Outline every leukocyte.
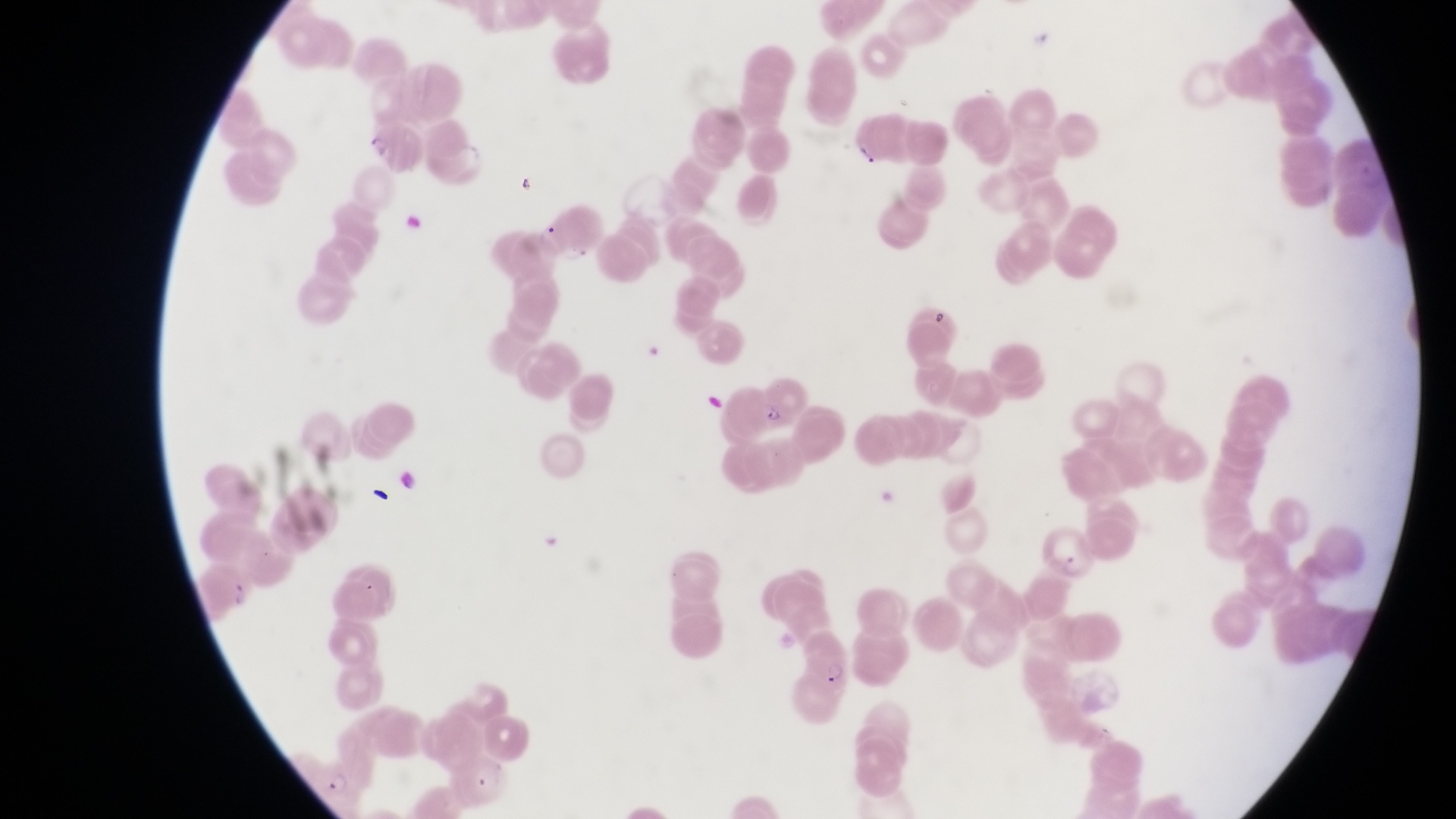
No leukocytes observed.

{
  "magnification": "1000x",
  "country": "Uganda",
  "preparation": "thin blood film",
  "field_of_view": "single",
  "artifact_platelet_like_body_stain_precipitate_or_debris_locations": "approximate bounding boxes as [left, top, right, bottom] in pixels: [856, 139, 883, 175], [512, 168, 545, 205], [925, 300, 958, 332], [367, 481, 399, 520]",
  "image_size": "1456×819 pixels",
  "parasitised_red_blood_cell_locations": "approximate bounding boxes as [left, top, right, bottom] in pixels: [753, 366, 808, 424], [798, 631, 851, 695]",
  "capture": "smartphone photograph through the eyepiece of an Olympus CX-23 microscope",
  "trophozoite_locations": "approximate bounding boxes as [left, top, right, bottom] in pixels: [314, 764, 359, 804]"
}